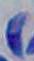

identification = Toxoplasma gondii
modality = micrograph
magnification = 1000x